Name the parasite shown.
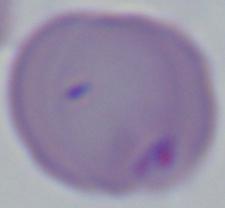
Babesia.

Summary:
  - Magnification: 1000x
  - Modality: photomicrograph